Report the malaria status of this cell.
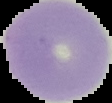

Uninfected.

From a thin blood film. Segmented cell region on a black background. Image is 112×103 pixels.